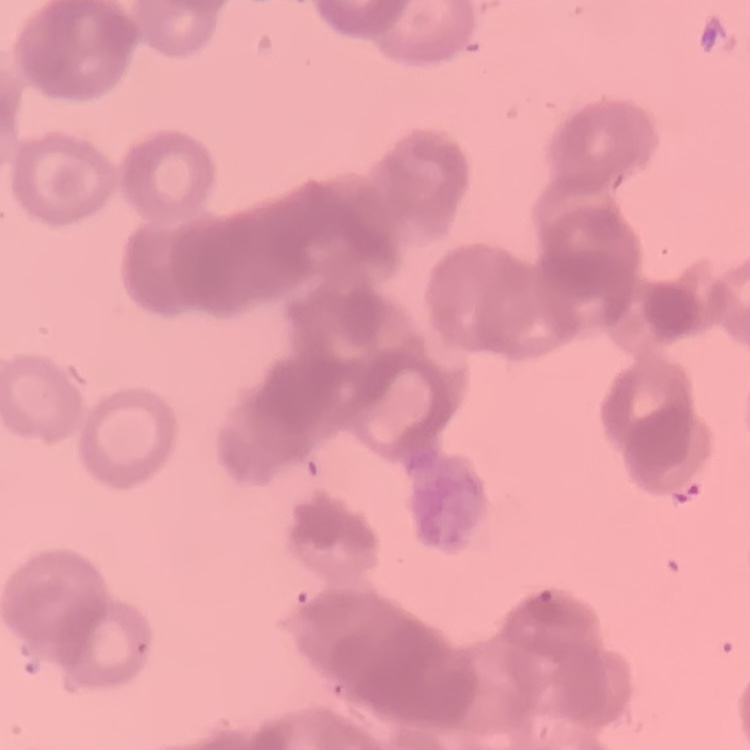
The red blood cells show rouleaux formation. Thin blood film. Field's or Giemsa stain. Square crop of a larger photomicrograph.